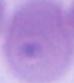
{
  "magnification": "1000x",
  "modality": "micrograph",
  "identification": "red blood cell"
}